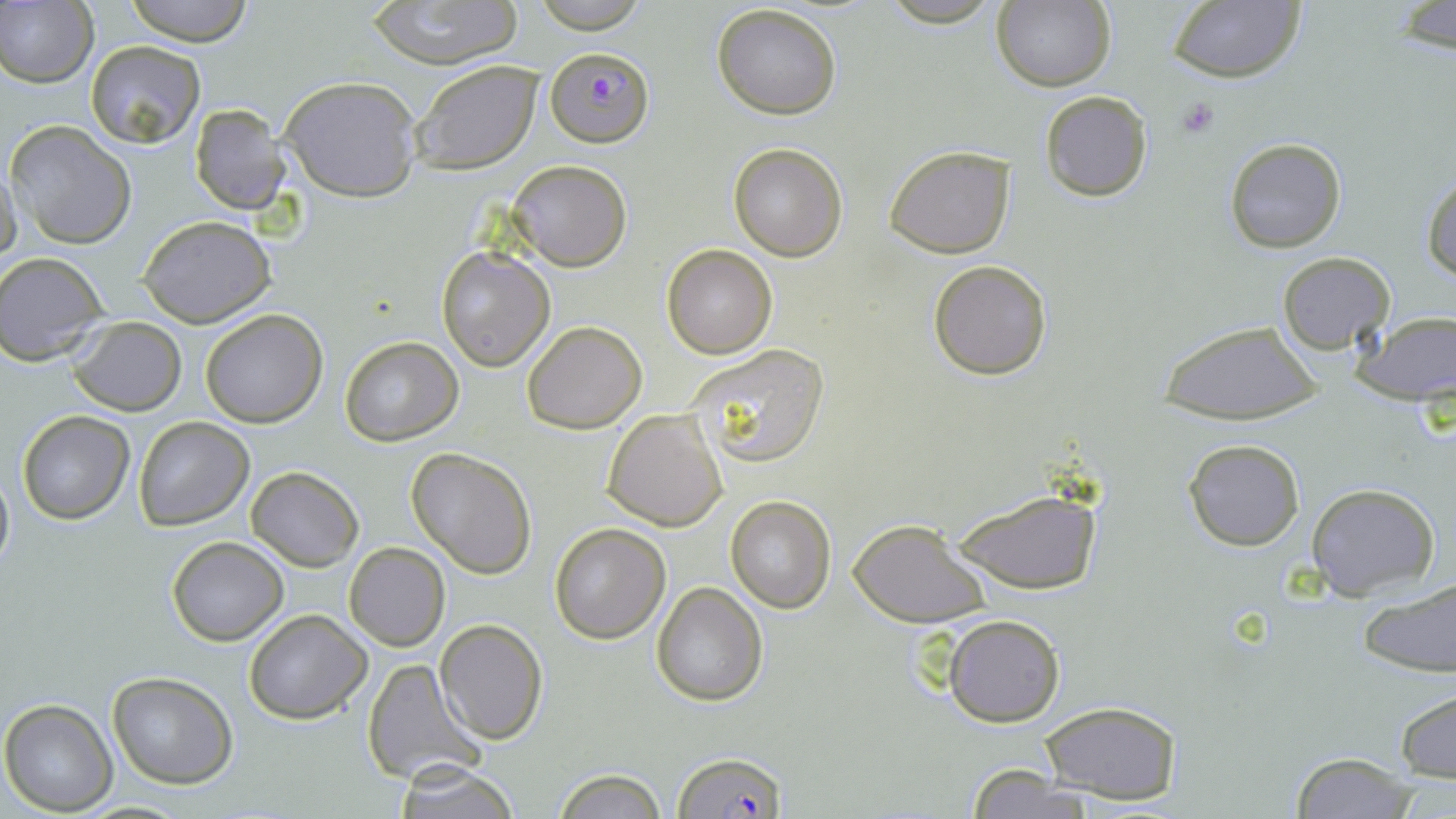
Approximate bounding boxes as named x1/y1/x2/y2 corners in pixels. Plasmodium falciparum-infected red blood cell locations: (x1=546, y1=46, x2=654, y2=148), (x1=673, y1=749, x2=788, y2=819). Platelet locations: (x1=1175, y1=94, x2=1223, y2=139). Uninfected red blood cell locations: (x1=0, y1=0, x2=97, y2=89), (x1=122, y1=0, x2=256, y2=45), (x1=369, y1=0, x2=521, y2=69), (x1=527, y1=0, x2=653, y2=34), (x1=1166, y1=0, x2=1306, y2=84), (x1=991, y1=1, x2=1115, y2=92), (x1=1393, y1=2, x2=1455, y2=55), (x1=712, y1=3, x2=842, y2=118), (x1=85, y1=40, x2=206, y2=148), (x1=410, y1=59, x2=543, y2=174), (x1=279, y1=75, x2=423, y2=203), (x1=1039, y1=91, x2=1153, y2=202), (x1=189, y1=104, x2=289, y2=213), (x1=6, y1=121, x2=137, y2=250), (x1=1224, y1=136, x2=1347, y2=254), (x1=727, y1=142, x2=848, y2=261), (x1=883, y1=144, x2=1017, y2=258), (x1=507, y1=160, x2=633, y2=271), (x1=0, y1=162, x2=22, y2=270), (x1=1422, y1=170, x2=1456, y2=281), (x1=137, y1=214, x2=277, y2=328), (x1=663, y1=244, x2=778, y2=360), (x1=436, y1=246, x2=555, y2=371), (x1=1276, y1=252, x2=1395, y2=354), (x1=0, y1=253, x2=108, y2=364), (x1=927, y1=259, x2=1053, y2=381), (x1=200, y1=309, x2=328, y2=427), (x1=1355, y1=310, x2=1456, y2=408), (x1=68, y1=316, x2=187, y2=417), (x1=522, y1=319, x2=647, y2=434), (x1=1159, y1=320, x2=1322, y2=425), (x1=338, y1=336, x2=463, y2=446), (x1=685, y1=343, x2=830, y2=468), (x1=601, y1=408, x2=728, y2=531), (x1=17, y1=412, x2=134, y2=524), (x1=132, y1=417, x2=253, y2=530), (x1=1183, y1=438, x2=1305, y2=550), (x1=406, y1=447, x2=537, y2=579), (x1=0, y1=464, x2=14, y2=579), (x1=246, y1=466, x2=363, y2=570), (x1=1307, y1=483, x2=1441, y2=600), (x1=952, y1=488, x2=1102, y2=593), (x1=725, y1=496, x2=835, y2=612), (x1=847, y1=517, x2=992, y2=628), (x1=549, y1=523, x2=671, y2=643), (x1=165, y1=536, x2=290, y2=646), (x1=344, y1=542, x2=450, y2=652), (x1=651, y1=581, x2=768, y2=707), (x1=1357, y1=582, x2=1456, y2=678), (x1=244, y1=609, x2=372, y2=725), (x1=943, y1=613, x2=1065, y2=728), (x1=434, y1=619, x2=548, y2=745), (x1=363, y1=659, x2=484, y2=786), (x1=106, y1=672, x2=238, y2=788), (x1=1395, y1=689, x2=1456, y2=784), (x1=0, y1=698, x2=119, y2=816), (x1=1039, y1=701, x2=1183, y2=805), (x1=1288, y1=751, x2=1419, y2=819), (x1=391, y1=761, x2=524, y2=819), (x1=965, y1=766, x2=1098, y2=819), (x1=552, y1=767, x2=668, y2=818). Slide-level diagnosis: Plasmodium falciparum. Optical microscopy. May-Grünwald-Giemsa-stained preparation. One field of a larger specimen. Thin blood smear. Image is 1456×819 pixels. 1000x magnification.